Assess this cell for malaria.
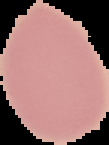
Uninfected.

preparation = thin blood smear
image size = 109×145 pixels
image type = cell region segmented out of the field of view; surrounding area masked to black